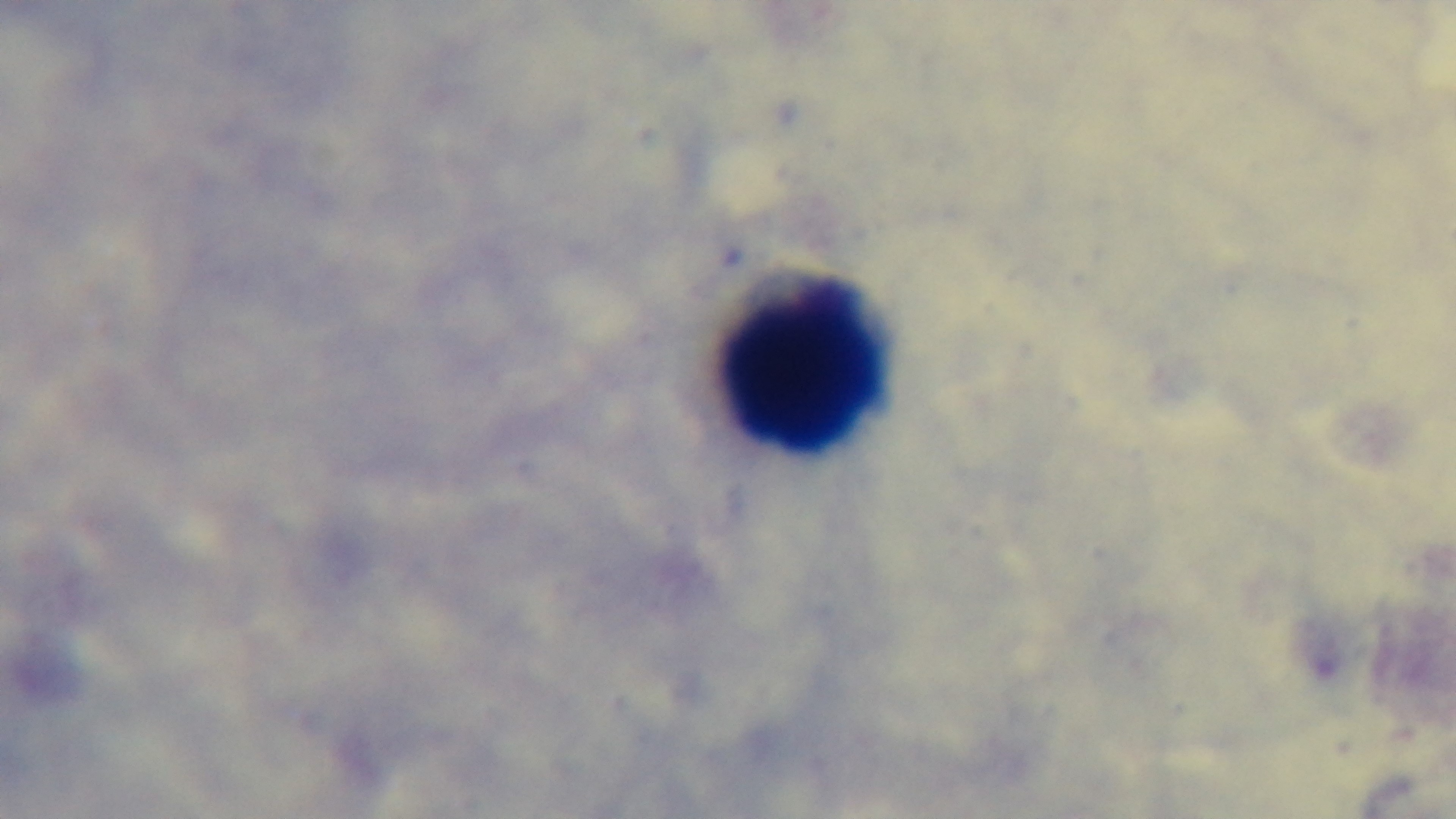

field_of_view: one from the slide
modality: light microscopy
stain: Giemsa
objective: 100x oil immersion
capture: mounted 4K digital camera
malaria_status: negative
preparation: thick